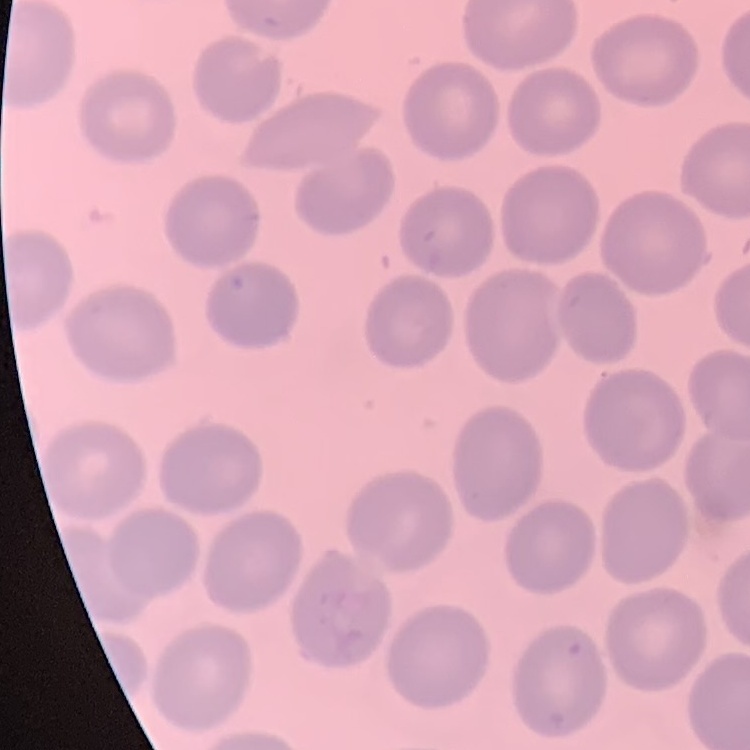
Summary:
  - Erythrocyte morphology: no rouleaux formation
  - Image type: square crop of a larger photomicrograph
  - Stain: Field's or Giemsa
  - Preparation: thin blood film